Report the malaria status of this cell.
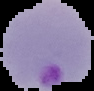

Parasitized.

preparation = thin blood film
image size = 94×91 pixels
image type = segmented cell region with the area outside set to black